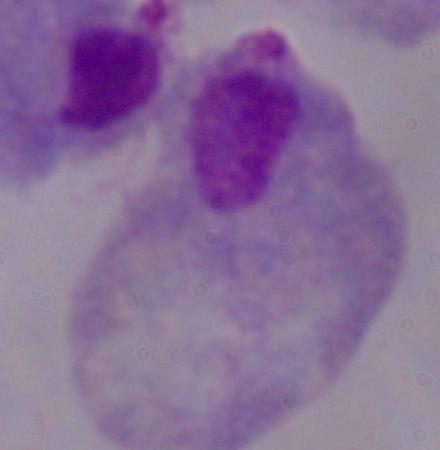

A trichomonad is seen. Micrograph. Captured at 1000x magnification.